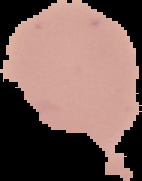
preparation: thin blood film
image_size: 142×181 pixels
image_type: segmented cell region with the area outside set to black
malaria_status: uninfected